Classify this cell by malaria status.
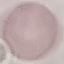
Uninfected.

Cell patch, automatically extracted from a larger field of view and resized to 64 × 64 pixels. Photographed with a smartphone camera at the microscope eyepiece. Thin blood film. Giemsa-stained preparation.